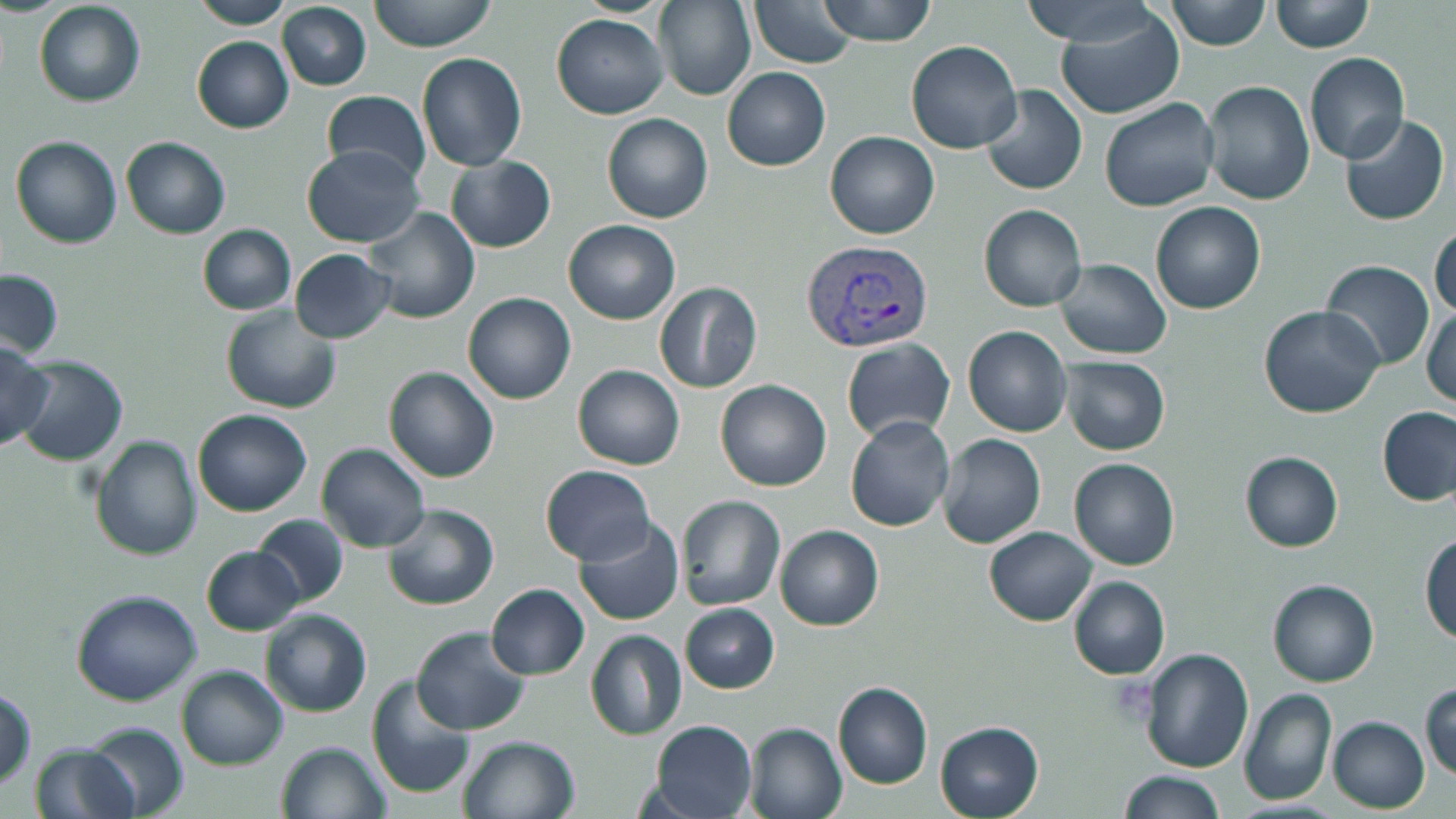

slide_level_diagnosis: Plasmodium vivax
platelet_locations: 'approximate bounding boxes as [x1, y1, x2, y2] in pixels: [1104, 673, 1163, 731]'
field_of_view: single
image_size: 1456×819 pixels
plasmodium_vivax_infected_red_blood_cell_locations: 'approximate bounding boxes as [x1, y1, x2, y2] in pixels: [801, 240, 932, 354]'
stain: May-Grünwald-Giemsa
modality: light microscopy
uninfected_red_blood_cell_locations: 'approximate bounding boxes as [x1, y1, x2, y2] in pixels: [197, 0, 290, 28], [367, 0, 498, 51], [655, 0, 754, 102], [817, 0, 940, 45], [1014, 0, 1167, 44], [1166, 0, 1271, 49], [1270, 0, 1374, 53], [751, 1, 859, 68], [34, 3, 146, 108], [279, 3, 371, 90], [1052, 9, 1183, 117], [552, 14, 669, 118], [192, 36, 294, 133], [907, 39, 1022, 153], [1305, 51, 1409, 163], [416, 52, 528, 172], [723, 68, 830, 171], [1203, 80, 1315, 206], [981, 85, 1088, 195], [322, 90, 432, 181], [1099, 97, 1220, 211], [1339, 112, 1449, 226], [603, 113, 713, 223], [826, 130, 940, 238], [11, 136, 124, 251], [121, 137, 232, 238], [302, 145, 422, 246], [446, 155, 557, 252], [1151, 202, 1266, 314], [979, 204, 1088, 311], [366, 207, 479, 323], [563, 218, 680, 326], [198, 224, 297, 315], [1430, 225, 1455, 320], [291, 249, 397, 344], [1057, 258, 1171, 359], [1321, 261, 1435, 369], [1, 271, 64, 358], [655, 282, 762, 394], [462, 292, 577, 403], [224, 303, 344, 415], [1259, 304, 1384, 418], [1422, 304, 1455, 410], [964, 326, 1074, 436], [0, 336, 53, 447], [842, 337, 954, 445], [14, 356, 128, 465], [1058, 356, 1170, 454], [573, 365, 684, 468], [384, 366, 499, 481], [716, 379, 830, 490], [1377, 406, 1454, 506], [194, 408, 312, 515], [845, 415, 955, 531], [937, 434, 1046, 548], [92, 435, 202, 559], [319, 443, 429, 552], [1241, 452, 1343, 550], [1069, 458, 1180, 570], [540, 464, 656, 564], [678, 495, 785, 612], [384, 504, 498, 610], [253, 511, 350, 607], [575, 514, 683, 625], [776, 525, 883, 631], [986, 527, 1096, 625], [1421, 535, 1455, 647], [204, 545, 301, 635], [1068, 576, 1170, 680], [1268, 580, 1378, 686], [486, 584, 589, 679], [73, 589, 204, 706], [682, 604, 778, 693], [262, 610, 371, 718], [414, 628, 530, 735], [586, 630, 686, 740], [1140, 647, 1255, 773], [177, 666, 287, 769], [366, 675, 477, 797], [833, 680, 933, 790], [1421, 683, 1456, 779], [0, 687, 35, 795], [1239, 688, 1337, 806], [1329, 717, 1429, 811], [647, 720, 758, 818], [934, 721, 1044, 818], [747, 724, 847, 819], [83, 726, 190, 818], [459, 735, 577, 819], [278, 741, 392, 819], [28, 743, 140, 819], [1118, 771, 1228, 819]'
magnification: 1000x
preparation: thin blood film